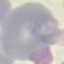
Malaria status: uninfected. Thin blood film. Photographed with a smartphone camera at the microscope eyepiece. Giemsa-stained preparation. Automatically extracted cell patch, resized to 64 × 64 pixels.